State the blood parasite species.
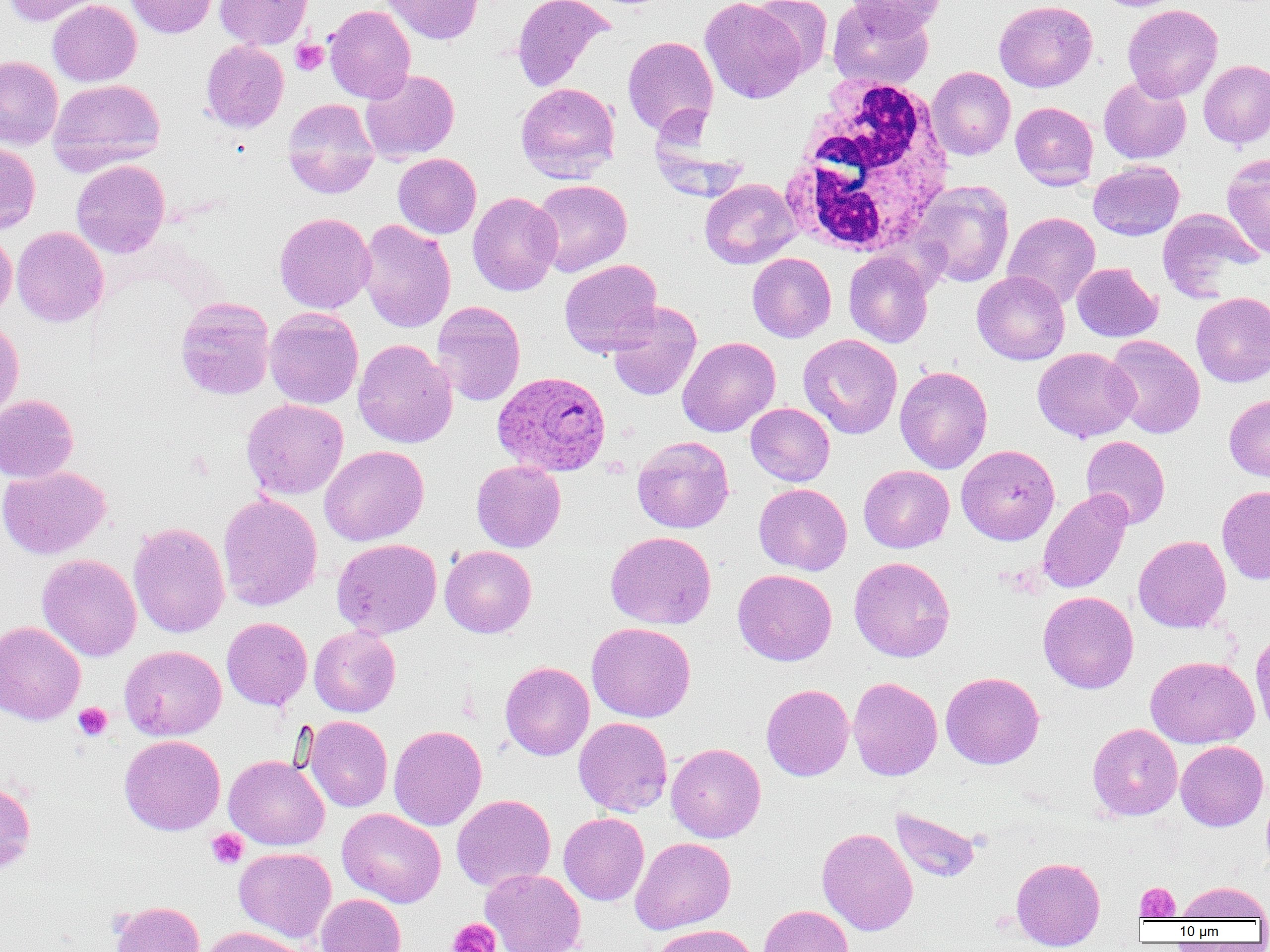
Plasmodium ovale.

Approximate bounding boxes as (x1,y1)-(x2,y2) corner pairs in pixels. White blood cell locations: (776,75)-(955,257). Uninfected red blood cell locations: (3,0)-(103,26), (48,0)-(141,86), (125,0)-(218,38), (215,0)-(313,49), (379,0)-(483,44), (512,0)-(613,92), (700,0)-(808,103), (749,0)-(833,77), (843,0)-(946,36), (994,0)-(1097,92), (828,1)-(933,90), (324,4)-(416,103), (1122,4)-(1223,101), (622,35)-(718,137), (200,40)-(289,133), (0,56)-(63,149), (1198,60)-(1270,148), (927,67)-(1015,160), (360,69)-(459,163), (1099,76)-(1191,164), (48,78)-(166,173), (516,82)-(620,181), (282,98)-(380,198), (1011,101)-(1098,190), (0,141)-(40,234), (393,153)-(481,238), (1221,153)-(1270,259), (71,159)-(170,258), (1088,161)-(1184,240), (700,178)-(801,269), (531,179)-(632,277), (911,179)-(1015,288), (467,191)-(562,295), (1157,208)-(1263,301), (274,212)-(376,314), (1002,212)-(1101,308), (357,220)-(456,333), (11,226)-(109,327), (0,228)-(17,320), (844,251)-(934,348), (747,253)-(836,342), (559,259)-(663,357), (1071,263)-(1162,342), (972,271)-(1070,365), (1191,292)-(1270,387), (175,297)-(275,400), (432,301)-(526,406), (607,301)-(702,401), (264,307)-(363,409), (0,317)-(24,423), (798,334)-(902,439), (1105,335)-(1205,439), (677,336)-(780,437), (353,338)-(457,448), (1033,347)-(1139,442), (894,366)-(993,474), (0,394)-(79,483), (1224,394)-(1270,482), (241,399)-(348,500), (745,403)-(835,486), (1081,435)-(1171,529), (632,436)-(735,533), (956,444)-(1060,545), (319,445)-(429,546), (471,461)-(565,552), (0,465)-(111,559), (858,465)-(954,553), (754,480)-(956,566), (753,483)-(852,575), (1217,485)-(1270,585), (1038,489)-(1132,594), (217,493)-(322,611), (128,522)-(230,639), (606,531)-(717,629), (1133,535)-(1231,633), (331,538)-(442,638), (440,545)-(536,638), (37,554)-(142,661), (848,556)-(955,662), (850,558)-(948,784), (733,569)-(837,666), (1038,591)-(1139,694), (222,618)-(312,710), (0,621)-(86,725), (586,622)-(696,722), (309,626)-(400,717), (1250,629)-(1270,736), (119,645)-(226,741), (1146,656)-(1259,748), (500,662)-(594,760), (941,671)-(1044,769), (847,677)-(942,781), (761,684)-(854,781), (304,716)-(393,812), (573,717)-(673,817), (1087,722)-(1183,820), (388,725)-(487,830), (573,731)-(766,826), (119,734)-(225,836), (1175,740)-(1269,831), (666,743)-(766,842), (223,754)-(330,850), (0,780)-(36,876), (451,794)-(555,891), (890,807)-(982,883), (337,808)-(446,908), (558,812)-(649,905), (817,827)-(918,935), (630,837)-(736,934), (234,847)-(336,943), (1011,856)-(1105,951), (480,868)-(586,952), (1175,881)-(1269,921), (315,893)-(406,952), (109,900)-(204,952), (758,905)-(854,952), (652,924)-(758,952), (200,926)-(308,952). Plasmodium ovale-infected red blood cell locations: (492,371)-(611,477). Platelet locations: (290,40)-(328,75), (73,703)-(112,741), (206,828)-(248,869), (1135,882)-(1180,921), (447,918)-(500,952). Single field of view. Captured at 1000x magnification. Thin blood film. Image is 1270×952 pixels. Light microscopy.